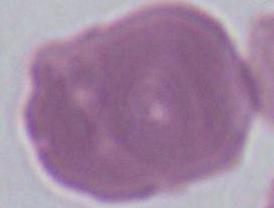
A red blood cell is shown. 1000x magnification. Photomicrograph.